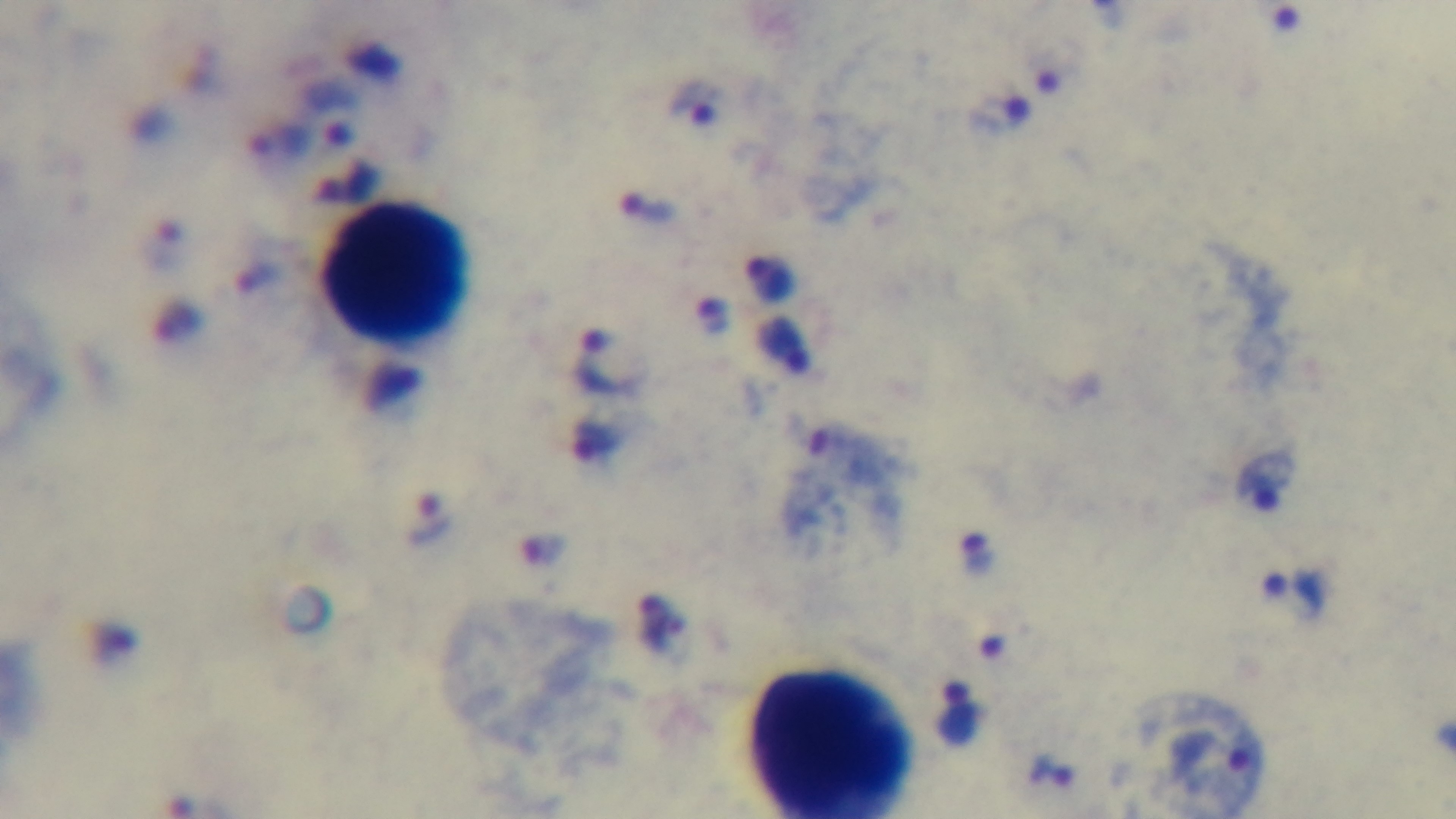

capture = mounted 4K digital camera
modality = light microscopy
objective = 100x oil immersion
malaria status = positive
field of view = one from the slide
preparation = thick smear
stain = Giemsa